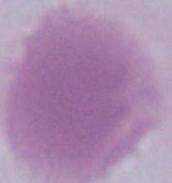
magnification = 1000x
modality = micrograph
identification = erythrocyte